Evaluate for malaria.
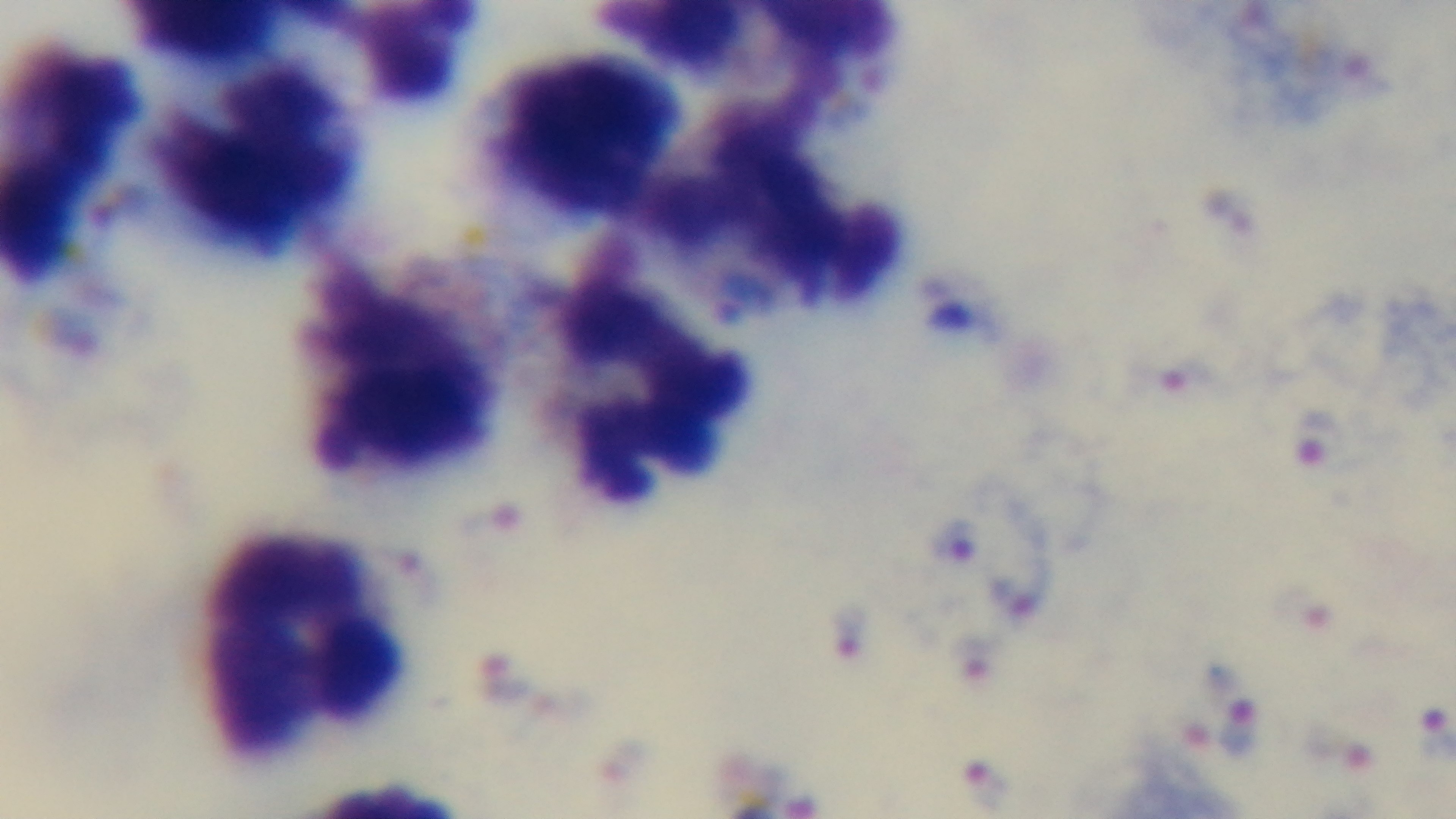
Positive.

modality: light microscopy
field_of_view: one from the slide
objective: 100x oil immersion
stain: Giemsa
capture: mounted 4K digital camera
preparation: thick smear